Comment on the morphology of the erythrocytes.
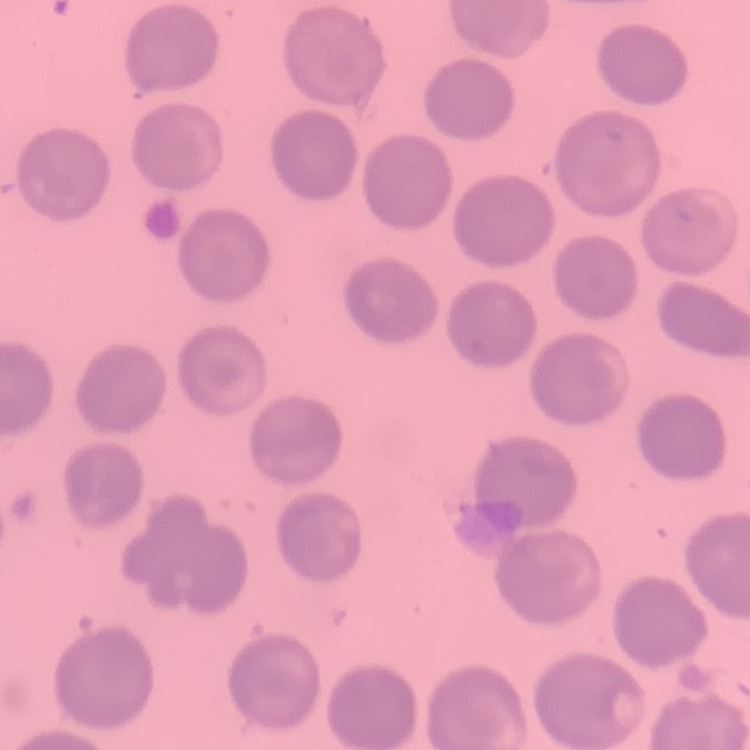
No rouleaux formation.

preparation: thin peripheral smear
stain: Field's or Giemsa
image_type: one tile cut from a larger photomicrograph